Classify this cell by malaria status.
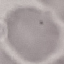
Uninfected.

Summary:
  - Preparation: thin blood smear
  - Stain: Giemsa
  - Capture: smartphone camera at the microscope eyepiece
  - Image type: automatically extracted cell patch, resized to 64 × 64 pixels